Classify this cell by malaria status.
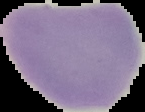
Uninfected.

Segmented cell region on a black background. From a thin blood smear. Image is 145×112 pixels.